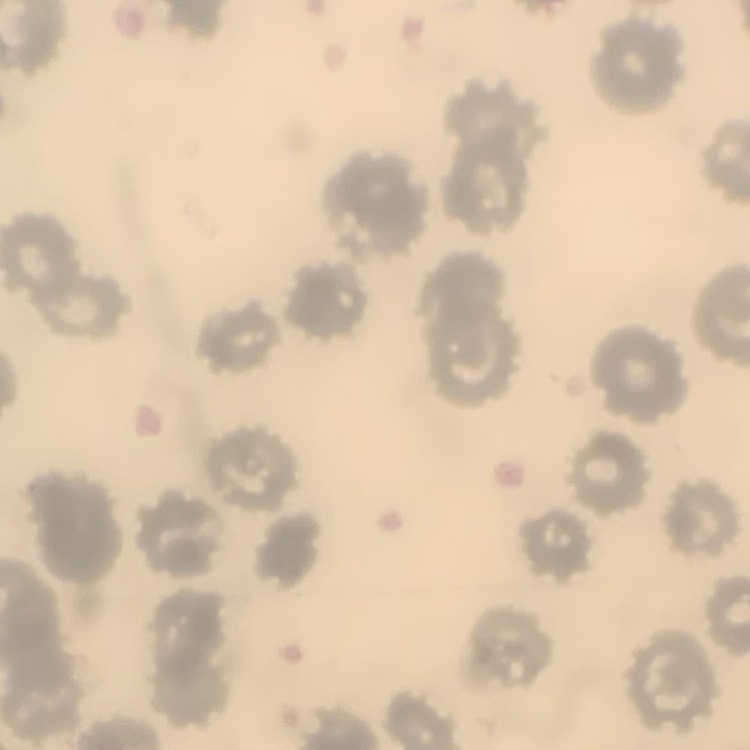
red_blood_cell_morphology: no rouleaux formation
preparation: thin blood smear
image_type: one tile cut from a larger photomicrograph
stain: Field's or Giemsa